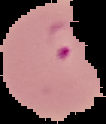

{
  "image_size": "106×124 pixels",
  "image_type": "cell region segmented out of the field of view; surrounding area masked to black",
  "result": "malaria parasites identified",
  "preparation": "thin blood smear"
}